State which parasite is depicted.
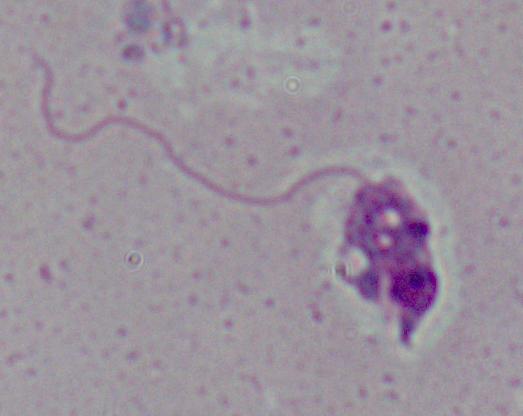
Leishmania.

modality: photomicrograph
magnification: 1000x